Look for parasitized red blood cells.
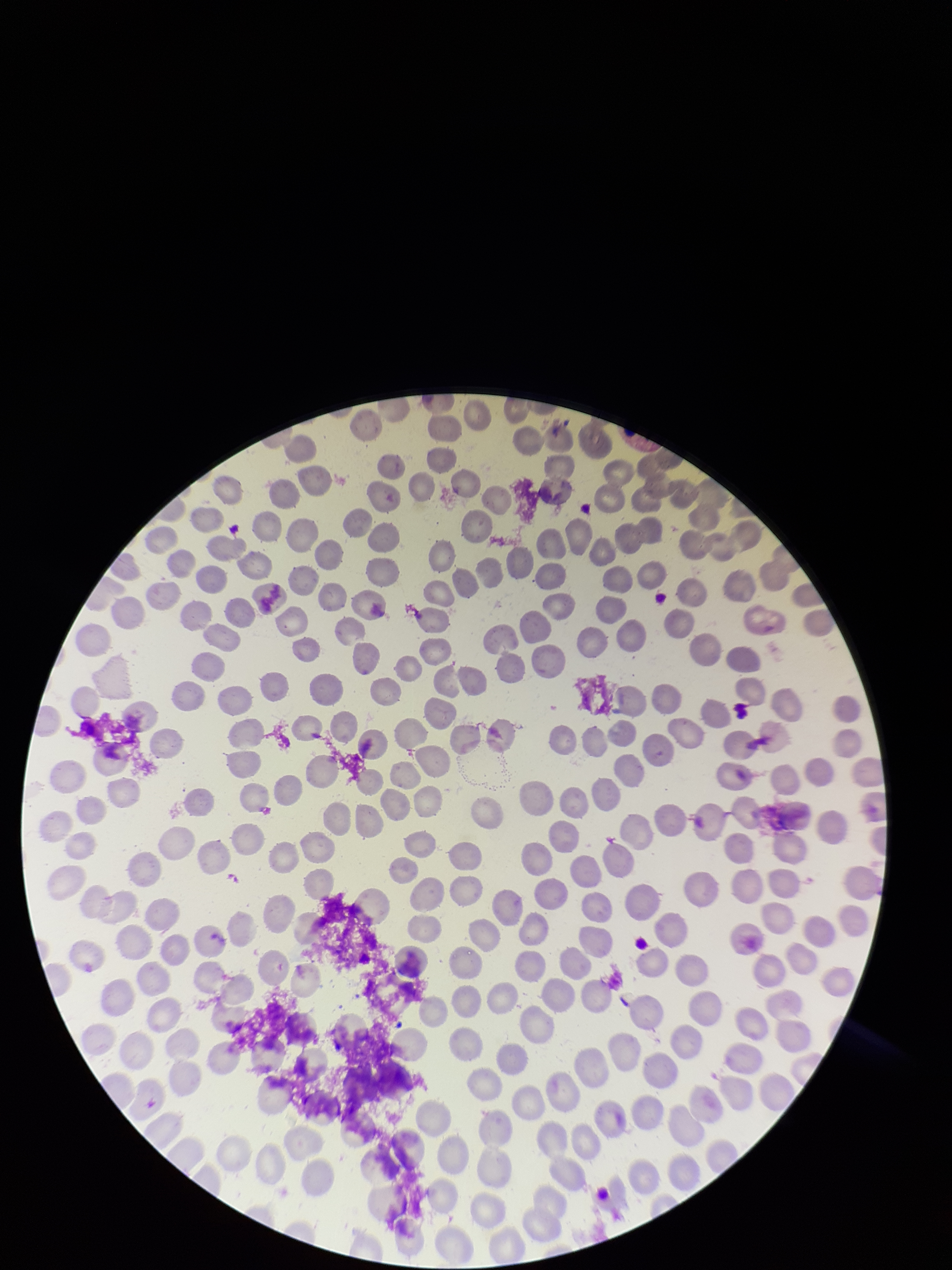
None detected.

Summary:
  - Image size: 952×1270 pixels
  - Parasitized red blood cell count: 0
  - Patient malaria status: negative
  - Field of view: single
  - Preparation: thin smear
  - Capture: smartphone photograph through the microscope eyepiece
  - Red blood cell count: 188
  - Stain: Giemsa